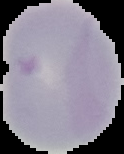

image size = 124×154 pixels
malaria status = uninfected
image type = segmented cell region on a black background
preparation = thin blood smear